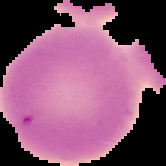
Summary:
  - Image type: segmented cell region on a black background
  - Malaria status: uninfected
  - Image size: 166×166 pixels
  - Preparation: thin blood film